Identify the parasite.
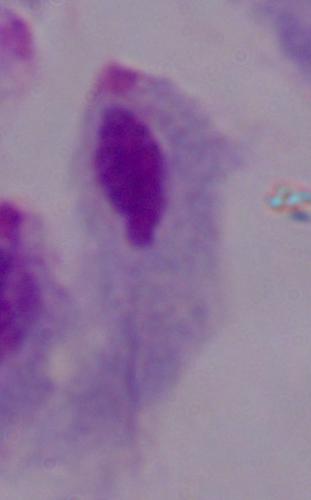

A trichomonad.

modality: photomicrograph
magnification: 1000x